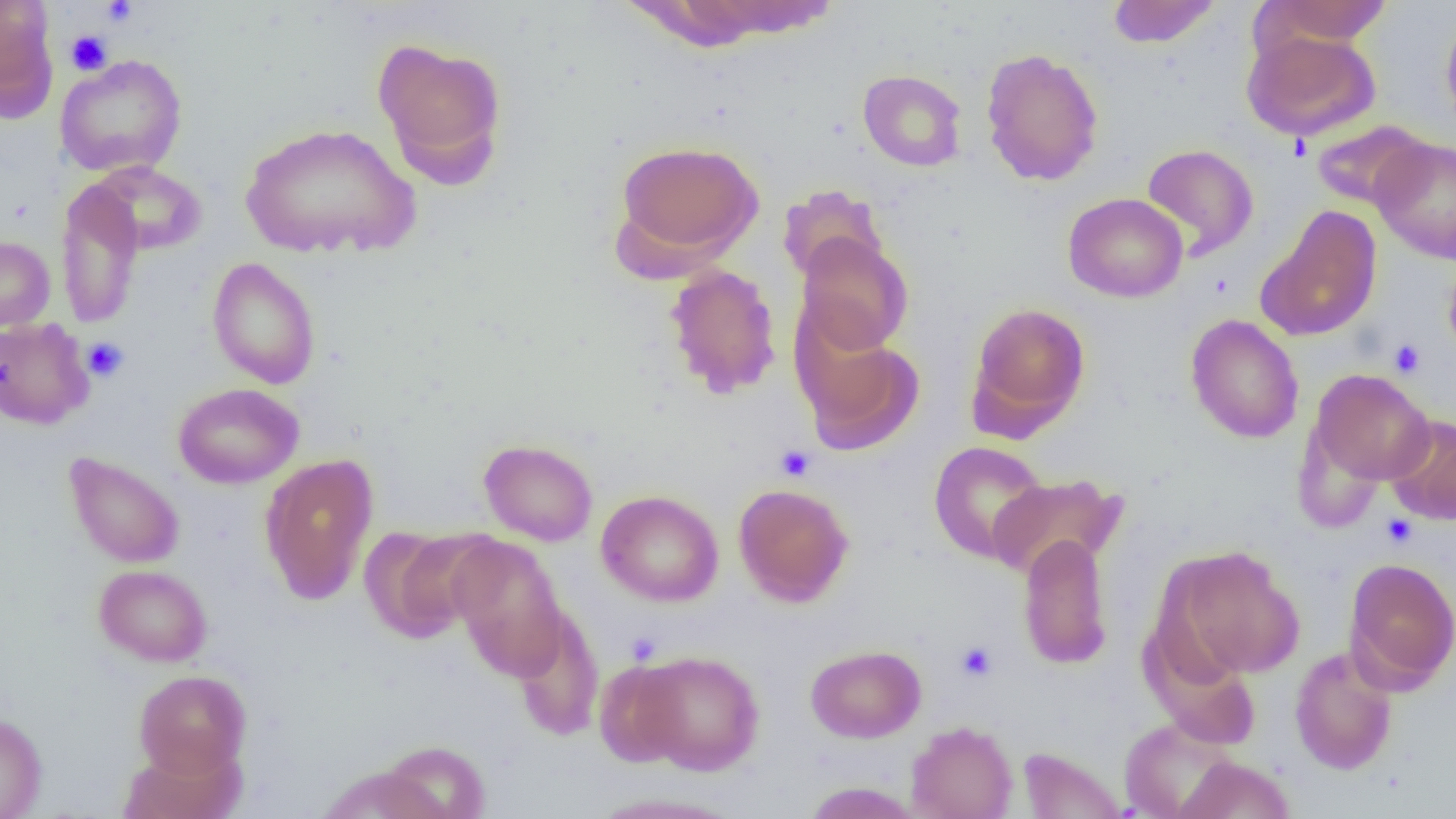

{
  "slide_level_diagnosis": "negative for blood parasites",
  "uninfected_red_blood_cell_locations": "approximate bounding boxes as (x1,y1)-(x2,y2) corner pairs in pixels: (1107,0)-(1221,49), (1263,0)-(1394,45), (0,1)-(58,119), (680,1)-(842,41), (1440,11)-(1456,139), (1242,28)-(1382,142), (371,36)-(509,185), (980,47)-(1104,187), (54,54)-(187,178), (858,69)-(967,171), (1310,119)-(1432,212), (240,122)-(421,261), (1370,137)-(1456,263), (612,139)-(764,266), (1141,143)-(1258,260), (88,161)-(207,256), (56,179)-(145,329), (777,185)-(889,286), (1063,193)-(1188,303), (1257,206)-(1382,342), (795,232)-(913,356), (0,235)-(55,331), (207,256)-(321,390), (1442,258)-(1456,360), (663,263)-(782,399), (965,301)-(1092,437), (1186,314)-(1304,444), (0,317)-(94,430), (793,317)-(926,455), (1306,369)-(1435,490), (173,383)-(304,488), (1385,414)-(1456,525), (479,438)-(598,546), (928,441)-(1052,564), (63,451)-(185,569), (259,453)-(379,605), (987,473)-(1126,581), (733,483)-(854,607), (596,489)-(724,607), (359,525)-(493,643), (1017,533)-(1114,670), (447,536)-(570,678), (1163,544)-(1305,681), (1343,557)-(1456,692), (93,564)-(212,667), (510,606)-(605,741), (806,644)-(926,742), (1289,645)-(1399,775), (632,650)-(765,775), (594,659)-(690,768), (133,670)-(252,778), (0,712)-(47,818), (1118,717)-(1240,818), (906,720)-(1018,819), (379,740)-(490,819), (119,741)-(245,819), (1016,746)-(1127,818), (1173,755)-(1296,819), (318,765)-(445,818), (801,782)-(925,818), (584,791)-(745,819)",
  "preparation": "thin blood film",
  "field_of_view": "one of a larger specimen",
  "modality": "light microscopy",
  "platelet_locations": "approximate bounding boxes as (x1,y1)-(x2,y2) corner pairs in pixels: (101,0)-(139,27), (65,29)-(112,75), (81,337)-(130,382), (1388,338)-(1426,378), (775,444)-(816,482), (1380,513)-(1418,549), (955,640)-(999,682)",
  "image_size": "1456×819 pixels",
  "magnification": "1000x"
}